Identify the cell.
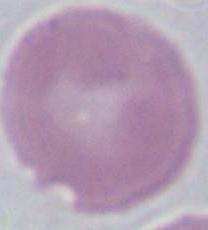
This is an erythrocyte.

modality = photomicrograph
magnification = 1000x